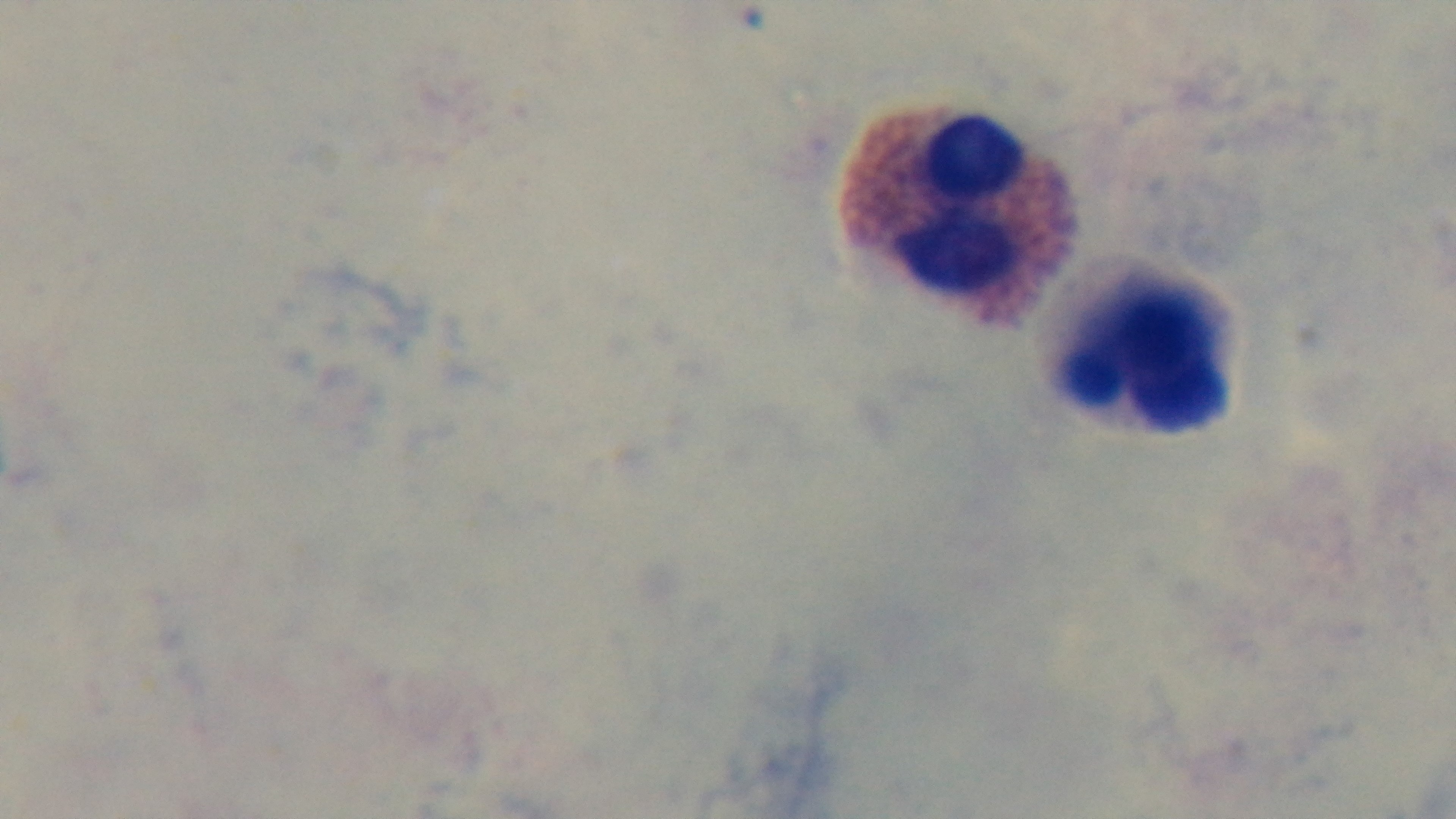

{
  "objective": "100x oil immersion",
  "malaria_status": "uninfected",
  "preparation": "thick",
  "modality": "light microscopy",
  "capture": "mounted 4K digital camera",
  "field_of_view": "single",
  "stain": "Giemsa"
}